Comment on the morphology of the erythrocytes.
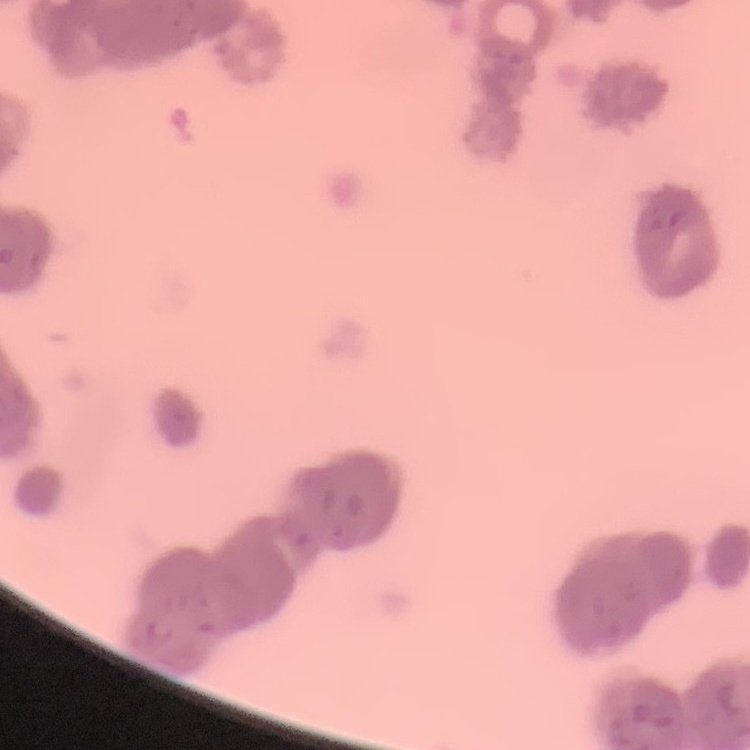
They show rouleaux formation.

Summary:
  - Stain: Field's or Giemsa
  - Preparation: thin peripheral smear
  - Image type: one tile cut from a larger photomicrograph